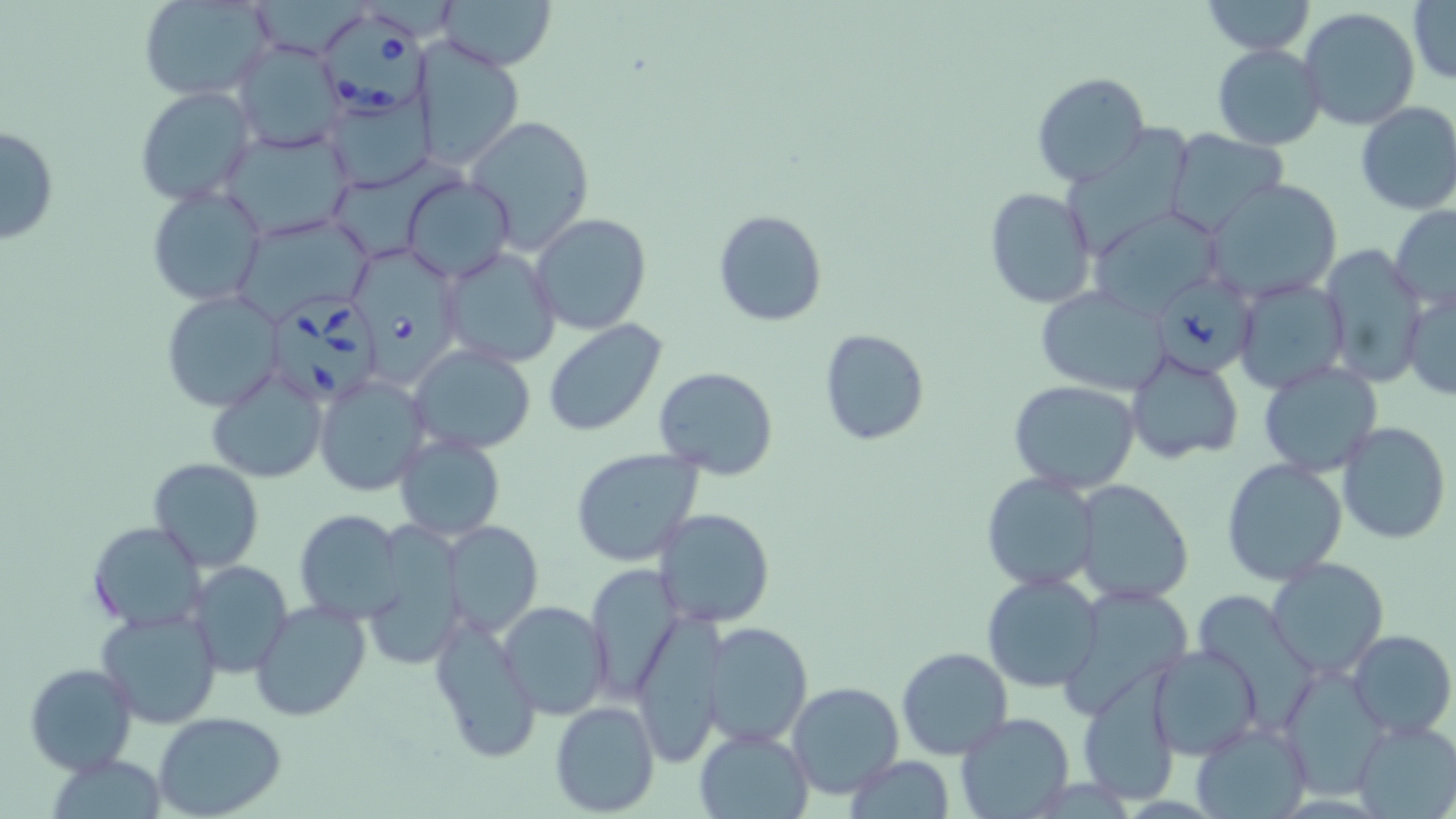
Approximate bounding boxes as named x1/y1/x2/y2 corners in pixels. Babesia divergens-infected red blood cell locations: (x1=316, y1=8, x2=437, y2=118), (x1=352, y1=244, x2=467, y2=383), (x1=1157, y1=268, x2=1261, y2=373), (x1=267, y1=292, x2=383, y2=406). Uninfected red blood cell locations: (x1=435, y1=0, x2=556, y2=72), (x1=1198, y1=0, x2=1317, y2=55), (x1=1407, y1=0, x2=1455, y2=85), (x1=138, y1=1, x2=274, y2=101), (x1=1298, y1=8, x2=1420, y2=130), (x1=231, y1=39, x2=345, y2=152), (x1=410, y1=39, x2=526, y2=169), (x1=1212, y1=43, x2=1326, y2=149), (x1=1030, y1=72, x2=1150, y2=189), (x1=134, y1=86, x2=255, y2=206), (x1=323, y1=88, x2=434, y2=191), (x1=1355, y1=102, x2=1456, y2=216), (x1=466, y1=115, x2=595, y2=254), (x1=0, y1=125, x2=59, y2=245), (x1=219, y1=128, x2=355, y2=241), (x1=1165, y1=129, x2=1288, y2=232), (x1=401, y1=175, x2=515, y2=281), (x1=1206, y1=180, x2=1342, y2=301), (x1=146, y1=184, x2=270, y2=309), (x1=983, y1=186, x2=1097, y2=310), (x1=1390, y1=204, x2=1456, y2=310), (x1=1087, y1=208, x2=1226, y2=317), (x1=713, y1=210, x2=827, y2=327), (x1=531, y1=213, x2=652, y2=335), (x1=235, y1=215, x2=374, y2=324), (x1=1318, y1=246, x2=1425, y2=387), (x1=439, y1=247, x2=562, y2=368), (x1=1233, y1=278, x2=1348, y2=395), (x1=1403, y1=287, x2=1456, y2=401), (x1=1035, y1=288, x2=1172, y2=396), (x1=160, y1=291, x2=287, y2=413), (x1=542, y1=320, x2=668, y2=437), (x1=819, y1=328, x2=929, y2=446), (x1=408, y1=344, x2=536, y2=454), (x1=1124, y1=350, x2=1244, y2=465), (x1=1258, y1=360, x2=1383, y2=477), (x1=652, y1=365, x2=780, y2=480), (x1=207, y1=369, x2=327, y2=486), (x1=314, y1=374, x2=429, y2=495), (x1=1010, y1=380, x2=1142, y2=494), (x1=1336, y1=421, x2=1451, y2=543), (x1=394, y1=433, x2=506, y2=540), (x1=571, y1=449, x2=706, y2=568), (x1=1222, y1=457, x2=1349, y2=587), (x1=149, y1=458, x2=263, y2=573), (x1=980, y1=472, x2=1101, y2=592), (x1=1073, y1=480, x2=1194, y2=603), (x1=653, y1=508, x2=777, y2=630), (x1=295, y1=510, x2=406, y2=625), (x1=444, y1=519, x2=542, y2=637), (x1=87, y1=522, x2=206, y2=632), (x1=359, y1=526, x2=468, y2=673), (x1=1266, y1=559, x2=1390, y2=679), (x1=187, y1=560, x2=295, y2=679), (x1=583, y1=566, x2=683, y2=701), (x1=981, y1=572, x2=1104, y2=692), (x1=250, y1=598, x2=374, y2=721), (x1=499, y1=600, x2=611, y2=718), (x1=99, y1=606, x2=223, y2=729), (x1=429, y1=606, x2=543, y2=764), (x1=629, y1=617, x2=728, y2=755), (x1=701, y1=622, x2=814, y2=748), (x1=1347, y1=629, x2=1456, y2=740), (x1=1149, y1=643, x2=1265, y2=760), (x1=897, y1=648, x2=1014, y2=760), (x1=24, y1=662, x2=137, y2=776), (x1=1279, y1=666, x2=1394, y2=800), (x1=1077, y1=676, x2=1182, y2=806), (x1=787, y1=682, x2=905, y2=799), (x1=549, y1=700, x2=661, y2=817), (x1=954, y1=710, x2=1074, y2=819), (x1=153, y1=712, x2=288, y2=819), (x1=1353, y1=716, x2=1456, y2=819), (x1=1191, y1=720, x2=1310, y2=818), (x1=694, y1=727, x2=811, y2=818), (x1=46, y1=751, x2=168, y2=818), (x1=844, y1=757, x2=955, y2=817). Slide-level diagnosis: Babesia divergens. Captured at 1000x magnification. Image is 1456×819 pixels. Single field of view. Optical microscopy. Thin blood film. May-Grünwald-Giemsa stain.